Assess this cell for malaria.
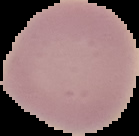

It is uninfected.

preparation = thin blood film
image size = 139×136 pixels
image type = cell region segmented out of the field of view; surrounding area masked to black